State which cell type is depicted.
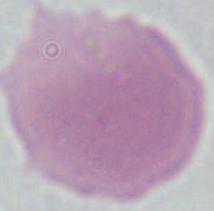
An erythrocyte.

1000x magnification. Photomicrograph.